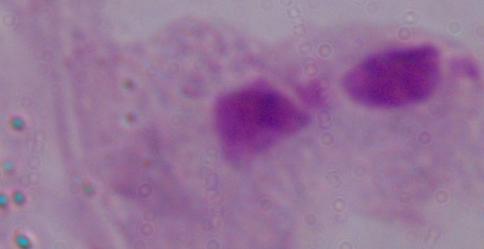

modality = micrograph
magnification = 1000x
identification = trichomonad